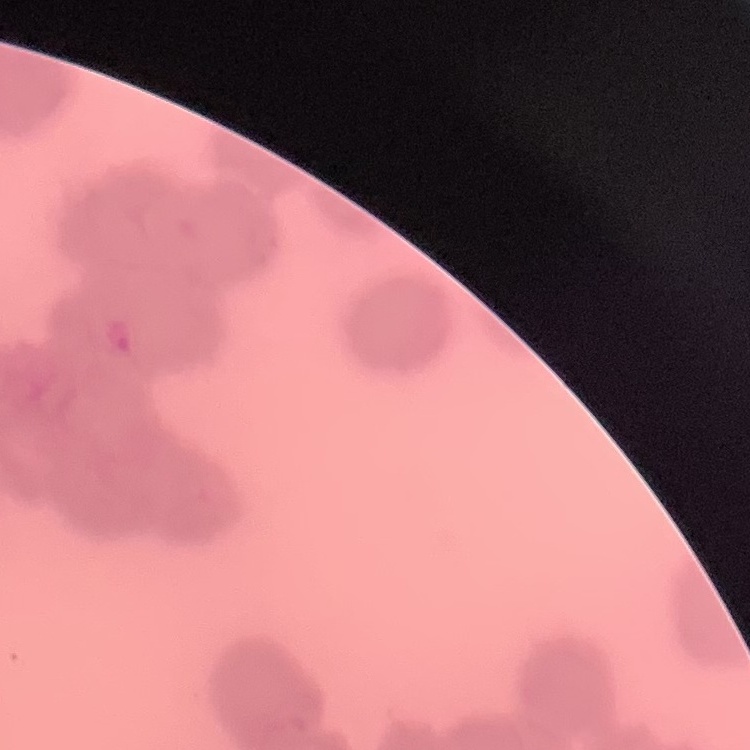

erythrocyte morphology = rouleaux formation
image type = one tile cut from a larger photomicrograph
stain = Field's or Giemsa
preparation = thin peripheral smear